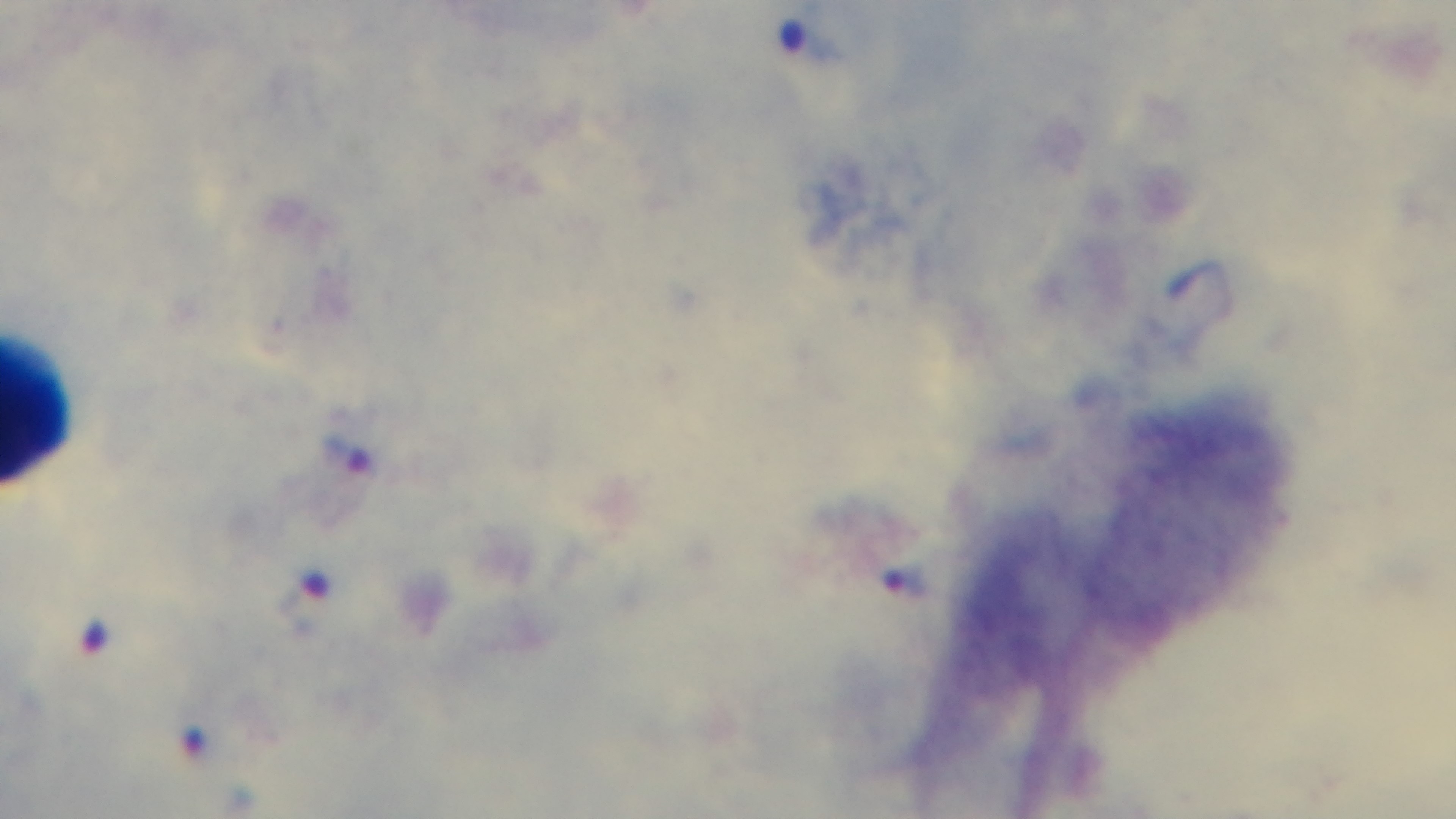
{
  "modality": "light microscopy",
  "capture": "mounted 4K digital camera",
  "preparation": "thick smear",
  "malaria_status": "infected",
  "objective": "100x oil immersion",
  "stain": "Giemsa",
  "field_of_view": "single"
}